Assess this cell for malaria.
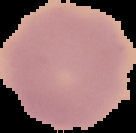

Uninfected.

image type = segmented cell region with the area outside set to black
preparation = thin blood film
image size = 136×133 pixels